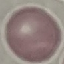

Result: no malaria parasites detected. Automatically extracted cell patch, resized to 64 × 64 pixels. Thin blood smear. Acquired by smartphone through the microscope eyepiece. Giemsa stain.